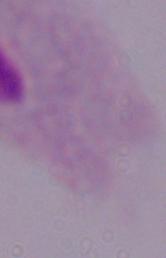

{
  "identification": "trichomonad",
  "magnification": "1000x",
  "modality": "micrograph"
}